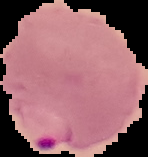

Summary:
  - Result: malaria parasites detected
  - Image size: 148×157 pixels
  - Preparation: thin blood smear
  - Image type: segmented cell region on a black background